Give the extent of all Plasmodium malariae-infected red blood cells.
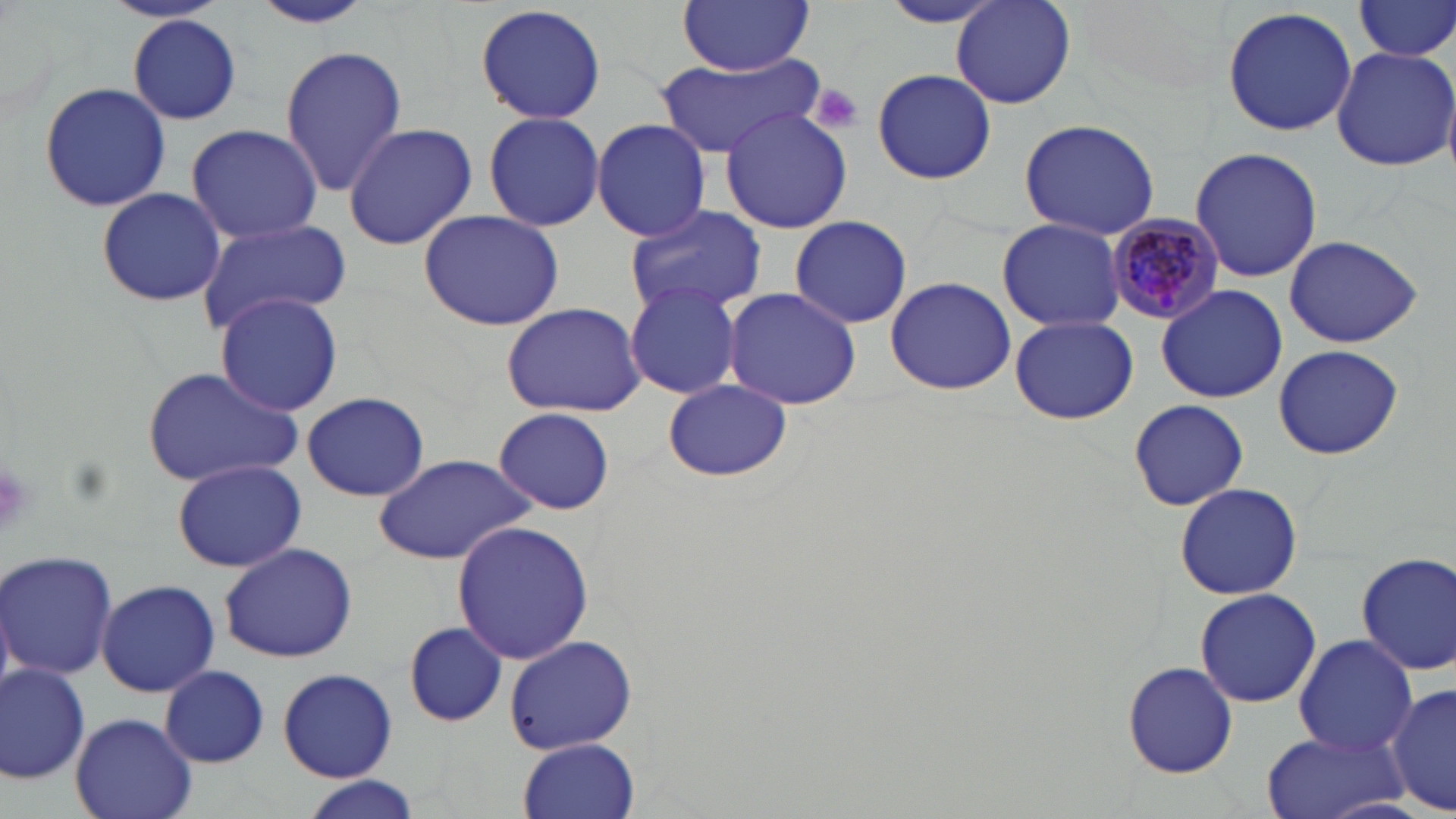

Approximate bounding boxes as [x1, y1, x2, y2] in pixels.
Plasmodium malariae-infected red blood cells: [1103, 217, 1226, 325].

{
  "slide_level_diagnosis": "Plasmodium malariae",
  "stain": "May-Grünwald-Giemsa",
  "modality": "light microscopy",
  "image_size": "1456×819 pixels",
  "field_of_view": "one of a larger specimen",
  "magnification": "1000x",
  "platelet_locations": "approximate bounding boxes as [x1, y1, x2, y2] in pixels: [807, 82, 866, 136], [0, 460, 31, 541]",
  "preparation": "thin blood smear",
  "uninfected_red_blood_cell_locations": "approximate bounding boxes as [x1, y1, x2, y2] in pixels: [101, 0, 232, 27], [676, 0, 815, 73], [952, 0, 1076, 109], [1354, 0, 1456, 61], [246, 1, 376, 29], [879, 2, 1007, 27], [475, 3, 608, 124], [1221, 6, 1358, 138], [128, 15, 243, 125], [279, 44, 408, 195], [1330, 46, 1456, 172], [655, 53, 823, 157], [871, 67, 995, 185], [38, 81, 171, 213], [720, 107, 852, 234], [483, 110, 605, 232], [592, 118, 711, 242], [1018, 118, 1161, 241], [185, 123, 324, 243], [341, 123, 478, 249], [1189, 146, 1322, 285], [96, 187, 226, 308], [622, 204, 768, 317], [417, 209, 565, 331], [788, 215, 914, 329], [996, 218, 1129, 333], [195, 219, 352, 334], [1283, 233, 1423, 348], [884, 278, 1017, 395], [625, 283, 741, 399], [1156, 284, 1287, 404], [722, 286, 862, 410], [214, 292, 344, 416], [500, 302, 647, 417], [162, 315, 331, 463], [1010, 316, 1138, 424], [1273, 343, 1403, 461], [140, 366, 302, 487], [663, 379, 792, 483], [298, 392, 432, 502], [1128, 399, 1247, 511], [494, 408, 618, 516], [373, 453, 538, 564], [173, 461, 306, 572], [1174, 482, 1303, 601], [450, 521, 593, 665], [217, 542, 360, 664], [1, 550, 118, 681], [1354, 551, 1456, 678], [95, 579, 220, 696], [1194, 588, 1321, 708], [402, 621, 510, 728], [504, 634, 638, 754], [1292, 634, 1419, 756], [1121, 660, 1239, 778], [0, 661, 93, 785], [160, 665, 270, 767], [277, 667, 398, 781], [1388, 682, 1454, 816], [71, 712, 197, 819], [1259, 729, 1408, 819], [519, 737, 640, 819], [295, 775, 425, 819]"
}